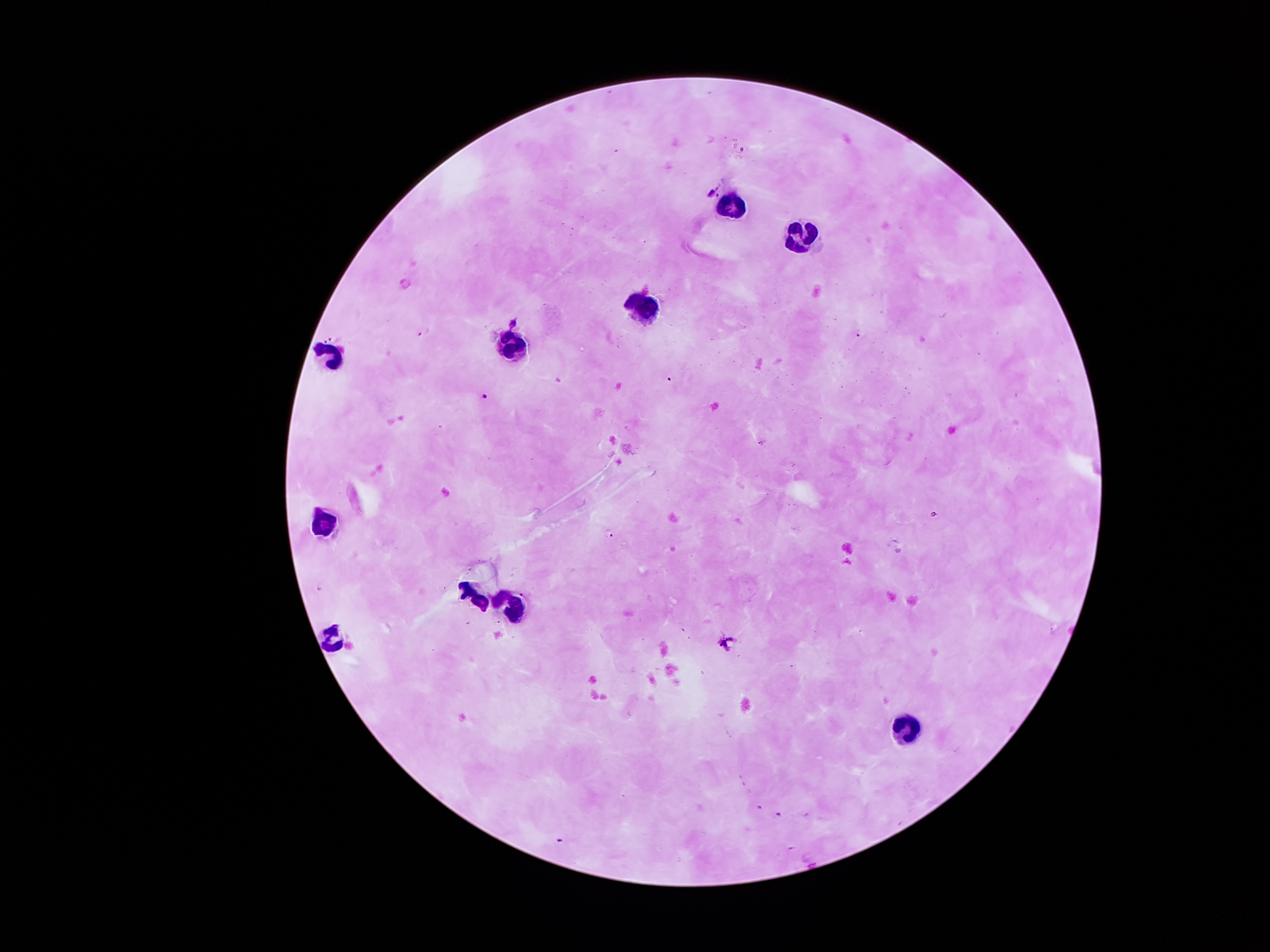
coordinate format = approximate centers as [x, y] in pixels
malaria parasite locations = [712, 193], [718, 196], [421, 334], [858, 336], [672, 379], [485, 396], [610, 534], [778, 814], [559, 841]
leukocyte locations = [729, 206], [810, 241], [645, 307], [517, 344], [335, 354], [321, 522], [471, 598], [507, 606], [336, 638], [904, 727]
patient malaria status = positive for Plasmodium falciparum
preparation = thick blood smear
stain = Giemsa
field of view = one from this slide
magnification = 100x
image size = 1270×952 pixels
capture = smartphone through the microscope eyepiece